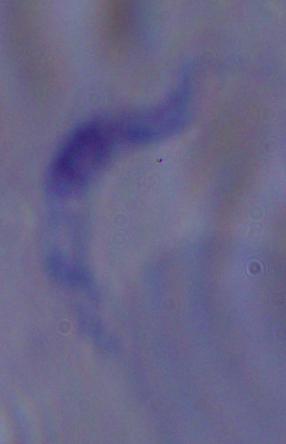

{
  "modality": "photomicrograph",
  "magnification": "1000x",
  "identification": "trypanosome"
}